Comment on the morphology of the red blood cells.
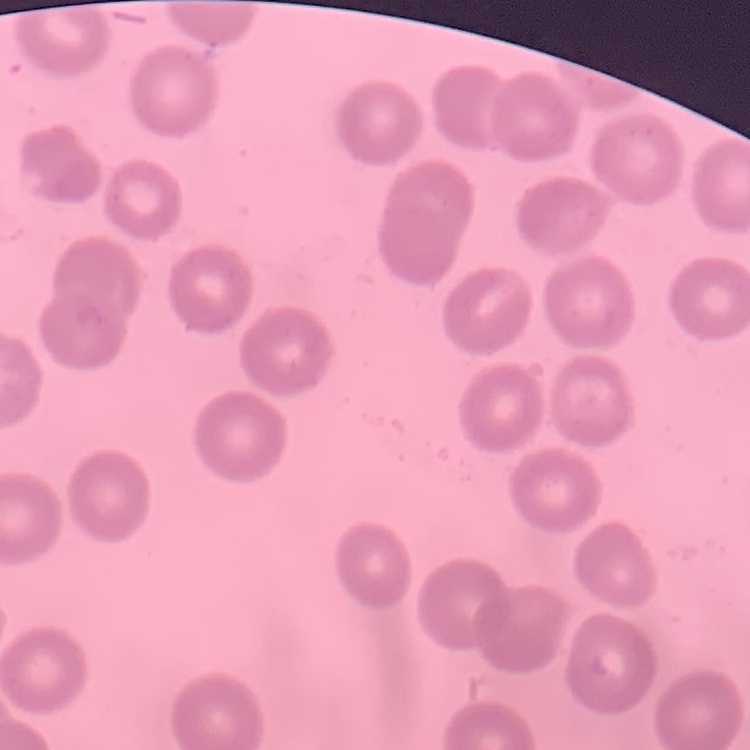

No rouleaux formation.

Thin blood film. Stained with either Field's or Giemsa. One tile cut from a larger photomicrograph.